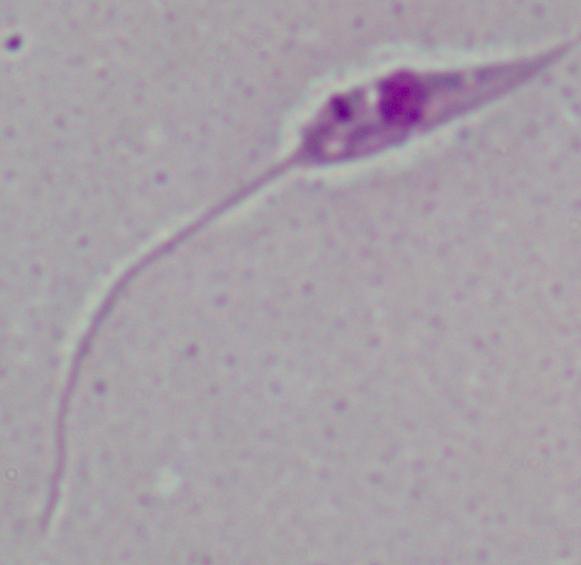

Summary:
  - Identification: Leishmania
  - Magnification: 1000x
  - Modality: micrograph